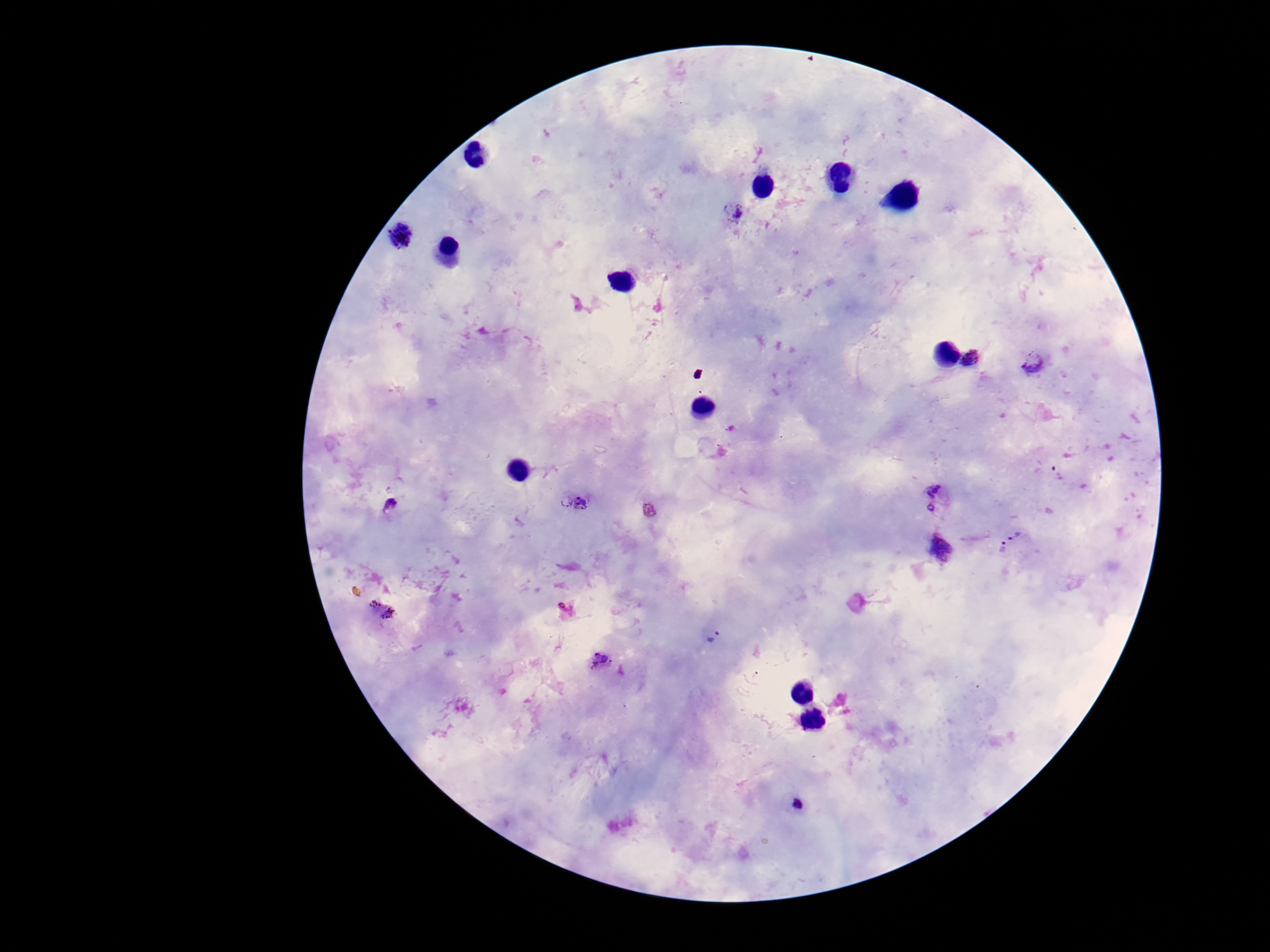
Approximate object centers, in pixels from the top-left corner. Plasmodium parasite locations: (x=733, y=211), (x=398, y=234), (x=971, y=359), (x=1033, y=362), (x=572, y=501), (x=934, y=501), (x=392, y=507), (x=653, y=513), (x=1017, y=534), (x=940, y=548), (x=1002, y=548), (x=380, y=608), (x=714, y=637), (x=599, y=659), (x=798, y=803). Thick peripheral-blood smear. Single field of view. Giemsa-stained preparation. 100x magnification. Image is 1270×952 pixels. Patient malaria status: positive. Smartphone photograph taken through the microscope eyepiece.